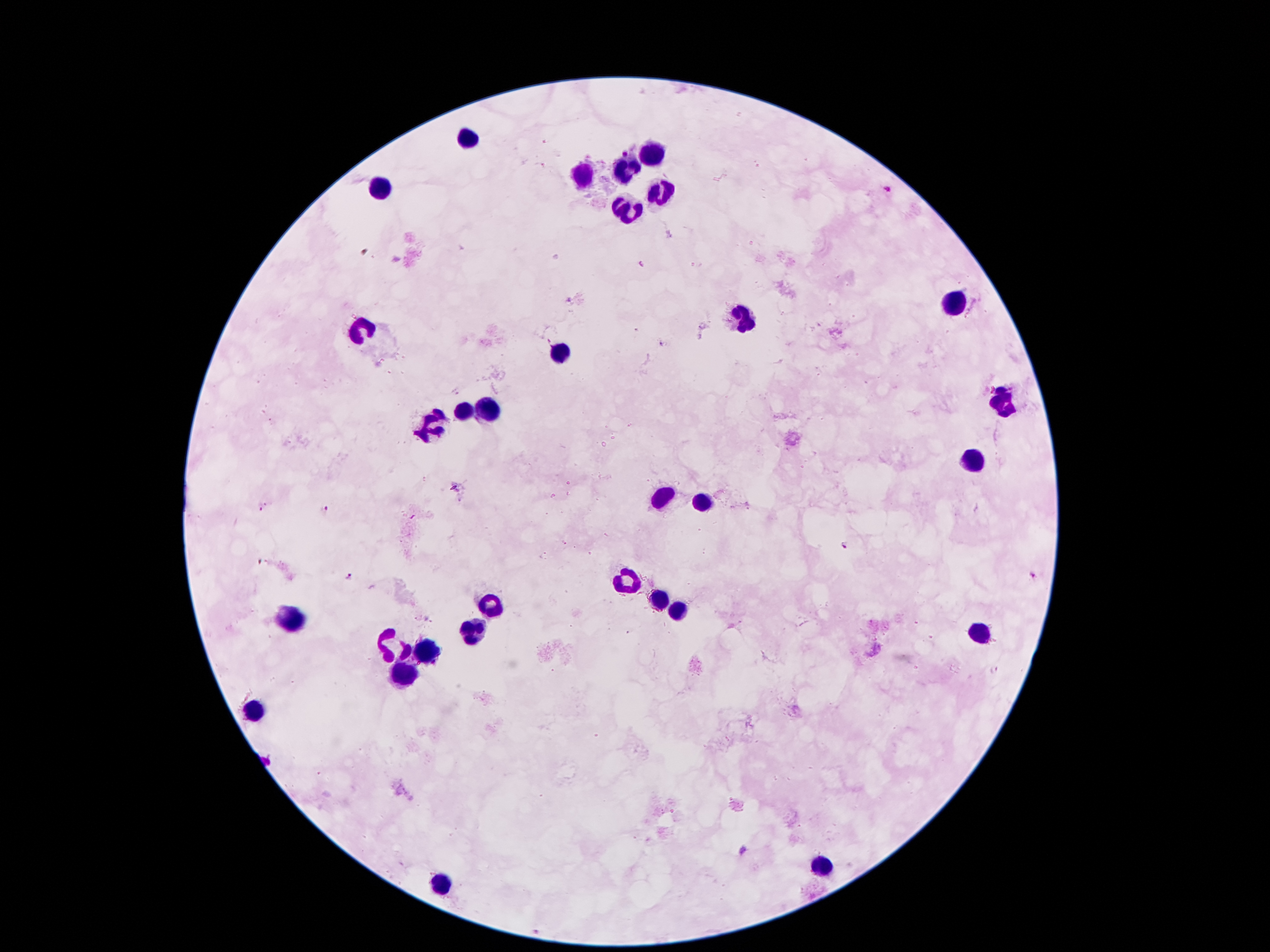

Approximate centers as [x, y] in pixels.
Summary:
  - Plasmodium parasite locations: [624, 149], [888, 188], [641, 264], [662, 343], [261, 508], [324, 510], [845, 545], [260, 562], [1032, 574], [348, 576], [995, 668]
  - Leukocyte locations: [468, 139], [650, 152], [625, 169], [583, 177], [382, 187], [661, 194], [629, 209], [953, 305], [743, 319], [360, 330], [556, 352], [1009, 400], [489, 412], [463, 415], [432, 427], [972, 463], [663, 499], [701, 501], [629, 579], [663, 599], [486, 606], [673, 609], [293, 618], [472, 634], [984, 634], [392, 642], [424, 653], [405, 674], [251, 712], [824, 864], [446, 884]
  - Magnification: 100x
  - Stain: Giemsa
  - Image size: 1270×952 pixels
  - Patient malaria status: infected with Plasmodium falciparum
  - Field of view: single
  - Preparation: thick blood smear
  - Capture: smartphone through the microscope eyepiece